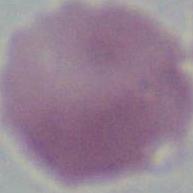
Summary:
  - Magnification: 1000x
  - Identification: red blood cell
  - Modality: photomicrograph